Assess this cell for malaria.
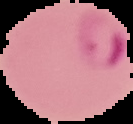
It is parasitized.

Image is 133×124 pixels. The area outside the segmented cell region is set to black. From a thin blood film.